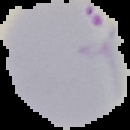

Result: Plasmodium parasites detected. Segmented cell region on a black background. Image is 130×130 pixels. From a thin blood smear.